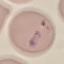

Summary:
  - Malaria status: parasitized
  - Stain: Giemsa
  - Image type: automatically extracted cell patch, resized to 64 × 64 pixels
  - Capture: smartphone camera at the microscope eyepiece
  - Preparation: thin smear